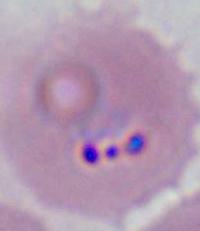

magnification: 400x or 1000x
modality: photomicrograph
identification: Plasmodium